Locate and identify every blood parasite.
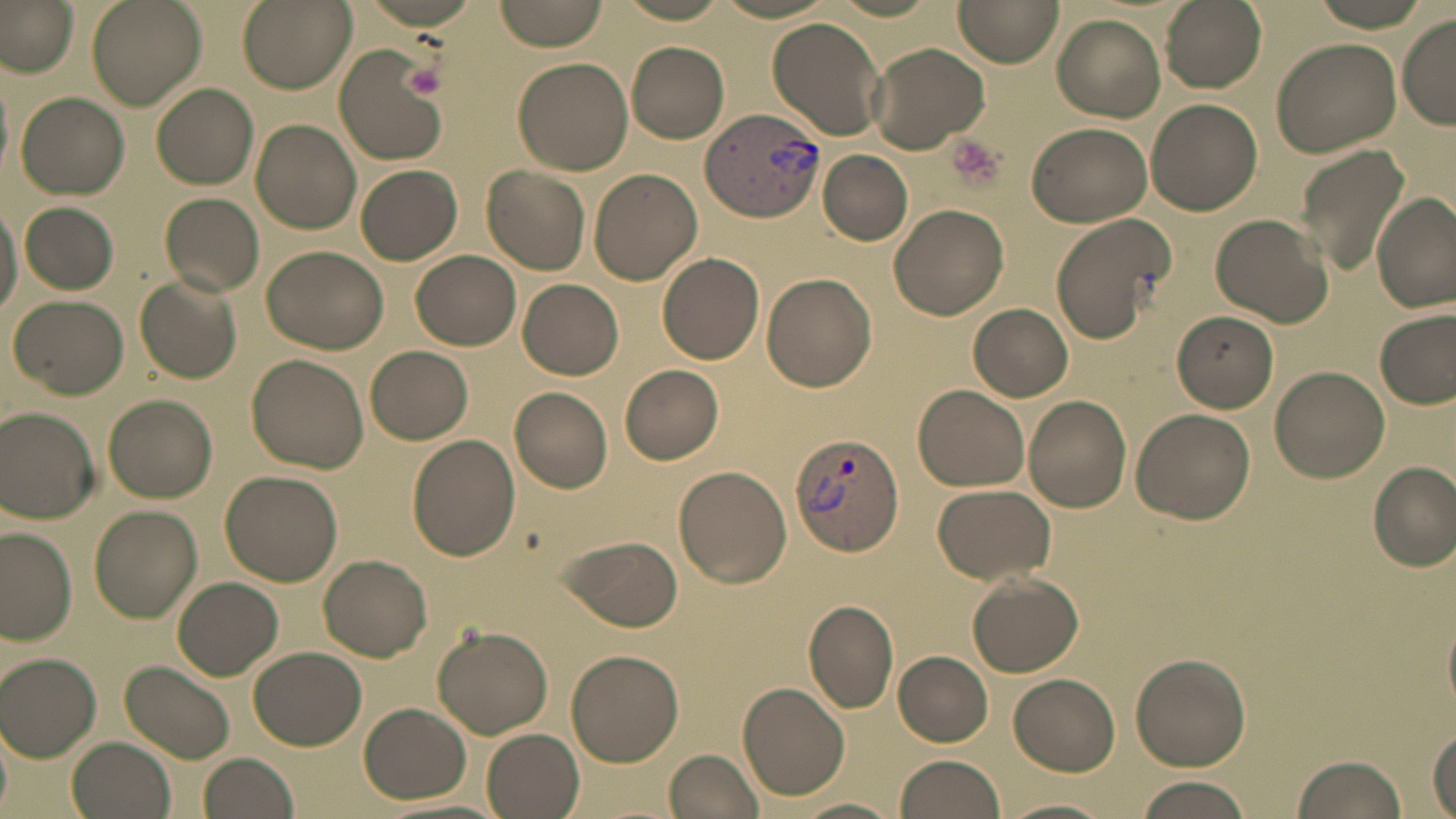
Approximate bounding boxes as (x1,y1)-(x2,y2) corner pairs in pixels.
Plasmodium vivax-infected red blood cells: (703,111)-(827,220), (789,432)-(905,555).
No Plasmodium falciparum, Plasmodium ovale, Plasmodium malariae, Babesia divergens, or Trypanosoma brucei observed.

Platelet locations: (402,62)-(447,98), (943,135)-(1006,192). Uninfected red blood cell locations: (89,0)-(206,110), (493,0)-(613,51), (955,0)-(1063,68), (1159,0)-(1266,92), (1,1)-(80,74), (237,1)-(354,92), (611,1)-(738,24), (706,1)-(846,23), (1051,14)-(1167,121), (1396,15)-(1456,128), (766,17)-(888,141), (1272,35)-(1407,157), (627,41)-(730,143), (866,41)-(990,153), (333,45)-(449,166), (513,54)-(634,175), (154,82)-(260,189), (17,92)-(130,199), (1145,98)-(1262,215), (251,119)-(361,234), (1026,122)-(1153,227), (1297,143)-(1411,277), (819,151)-(913,246), (354,165)-(462,264), (483,165)-(590,274), (588,168)-(703,285), (0,192)-(21,323), (160,193)-(264,296), (1372,193)-(1455,311), (20,201)-(118,295), (888,204)-(1009,321), (1048,210)-(1175,344), (1210,212)-(1334,327), (261,244)-(386,353), (410,250)-(521,351), (658,252)-(765,365), (762,272)-(878,391), (136,276)-(242,382), (517,278)-(624,379), (9,293)-(129,399), (968,304)-(1073,401), (1375,309)-(1456,411), (1172,311)-(1279,412), (366,346)-(473,444), (246,354)-(369,475), (620,365)-(724,465), (1271,365)-(1389,481), (913,383)-(1031,491), (509,386)-(613,494), (103,395)-(216,502), (1024,396)-(1132,512), (0,407)-(100,522), (1132,409)-(1258,525), (408,434)-(521,560), (1368,460)-(1455,571), (673,466)-(791,588), (221,470)-(342,585), (932,484)-(1056,584), (90,505)-(203,622), (0,527)-(77,644), (555,533)-(683,633), (319,554)-(433,660), (965,571)-(1084,678), (173,576)-(283,681), (804,600)-(899,714), (1442,607)-(1456,711), (432,626)-(557,737), (249,647)-(367,751), (565,649)-(684,767), (893,651)-(993,745), (1,653)-(102,762), (1132,653)-(1250,770), (122,661)-(236,763), (1009,674)-(1120,774), (738,681)-(851,801), (359,702)-(472,804), (0,723)-(12,818), (1428,727)-(1454,818), (482,729)-(585,818), (67,735)-(175,819), (663,749)-(766,819), (198,753)-(299,819), (1289,753)-(1409,819), (894,754)-(1007,819), (1132,778)-(1253,818), (1002,795)-(1119,819), (792,797)-(905,818). Slide-level diagnosis: Plasmodium vivax. May-Grünwald-Giemsa-stained preparation. Thin blood film. Image is 1456×819 pixels. Optical microscopy. One field of a larger specimen. Captured at 1000x magnification.